Classify this cell by malaria status.
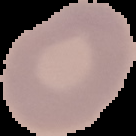
Uninfected.

{
  "image_size": "136×136 pixels",
  "image_type": "cell region segmented out of the field of view; surrounding area masked to black",
  "preparation": "thin blood smear"
}